Identify the parasite.
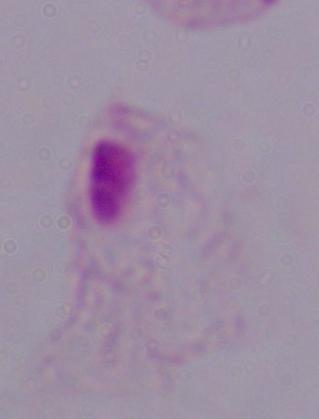
This is a trichomonad.

Micrograph. 1000x magnification.